Locate every blood parasite and identify its species.
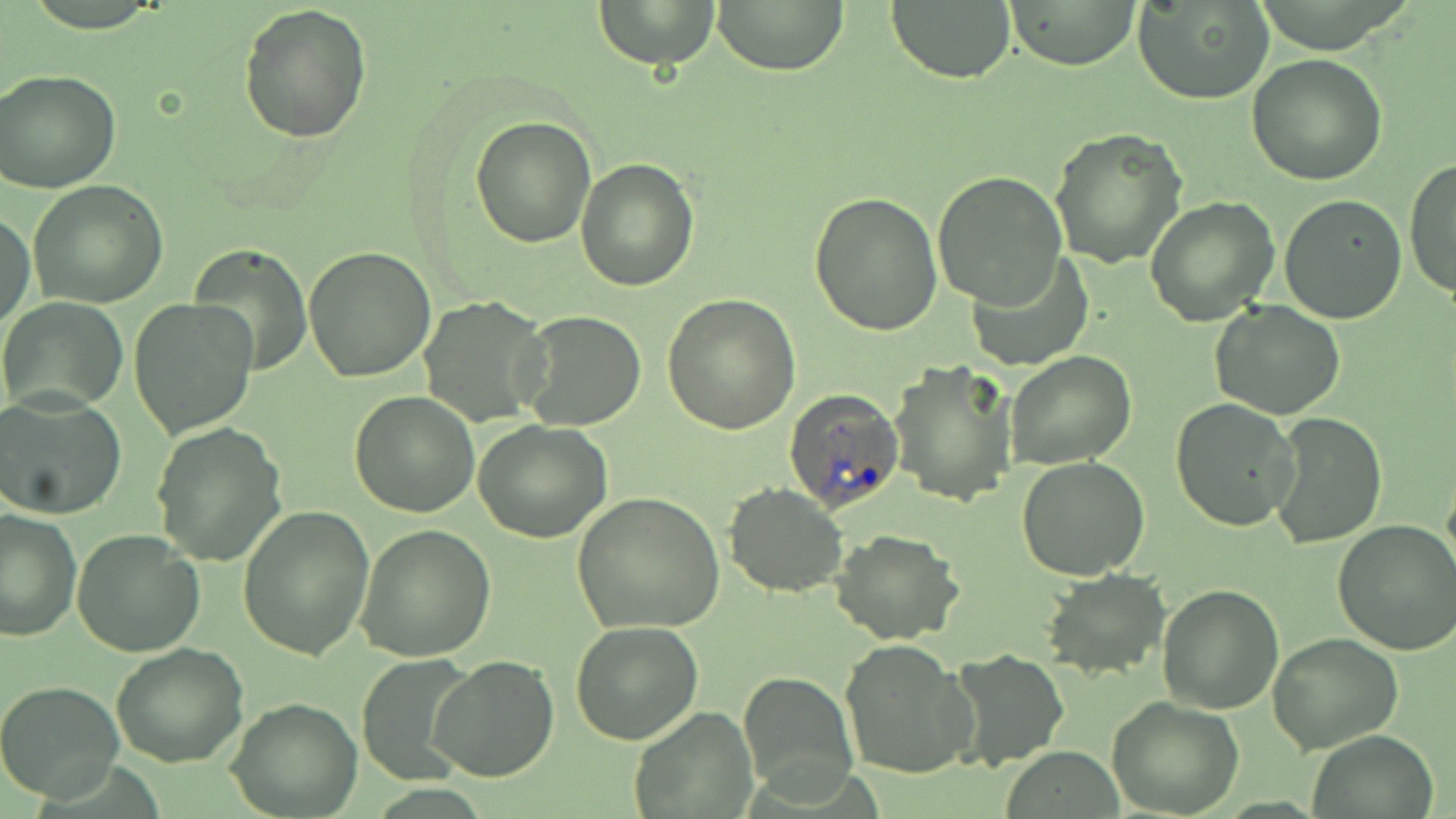

Approximate bounding boxes as (x1,y1)-(x2,y2) corner pairs in pixels.
Plasmodium ovale-infected red blood cells: (782,388)-(905,514).
No Plasmodium falciparum, Plasmodium malariae, Plasmodium vivax, Babesia divergens, or Trypanosoma brucei observed.

Uninfected red blood cell locations: (593,0)-(721,69), (712,0)-(850,74), (887,0)-(1016,84), (1006,1)-(1142,69), (1134,1)-(1276,104), (238,2)-(372,143), (1247,54)-(1388,186), (0,68)-(121,193), (471,115)-(597,249), (1049,129)-(1186,269), (1404,156)-(1456,301), (576,159)-(699,292), (932,170)-(1068,309), (27,180)-(168,308), (808,191)-(942,337), (1144,194)-(1281,328), (1277,194)-(1406,324), (1,213)-(35,331), (188,245)-(313,378), (303,245)-(436,381), (966,255)-(1093,371), (660,292)-(803,434), (418,295)-(551,426), (0,296)-(127,413), (129,297)-(258,440), (1212,300)-(1346,419), (518,308)-(648,431), (1004,350)-(1137,470), (890,359)-(1020,507), (348,390)-(479,517), (0,394)-(127,520), (1170,398)-(1301,532), (1269,413)-(1387,549), (474,419)-(612,542), (151,421)-(288,567), (1016,456)-(1150,580), (723,483)-(848,597), (571,492)-(725,633), (237,505)-(373,661), (0,508)-(82,644), (1333,518)-(1456,657), (356,524)-(496,662), (72,528)-(205,660), (831,528)-(966,645), (1038,568)-(1170,679), (1157,583)-(1285,715), (571,621)-(703,745), (1268,633)-(1403,753), (838,638)-(976,779), (111,642)-(249,769), (948,650)-(1069,769), (430,656)-(559,782), (353,657)-(480,782), (738,671)-(858,800), (0,681)-(125,802), (226,697)-(361,818), (1105,697)-(1246,818), (629,707)-(756,816), (1304,731)-(1441,819). Slide-level diagnosis: Plasmodium ovale. Captured at 1000x magnification. Thin blood film. Light microscopy. Image is 1456×819 pixels. One field of a larger specimen. May-Grünwald-Giemsa-stained preparation.